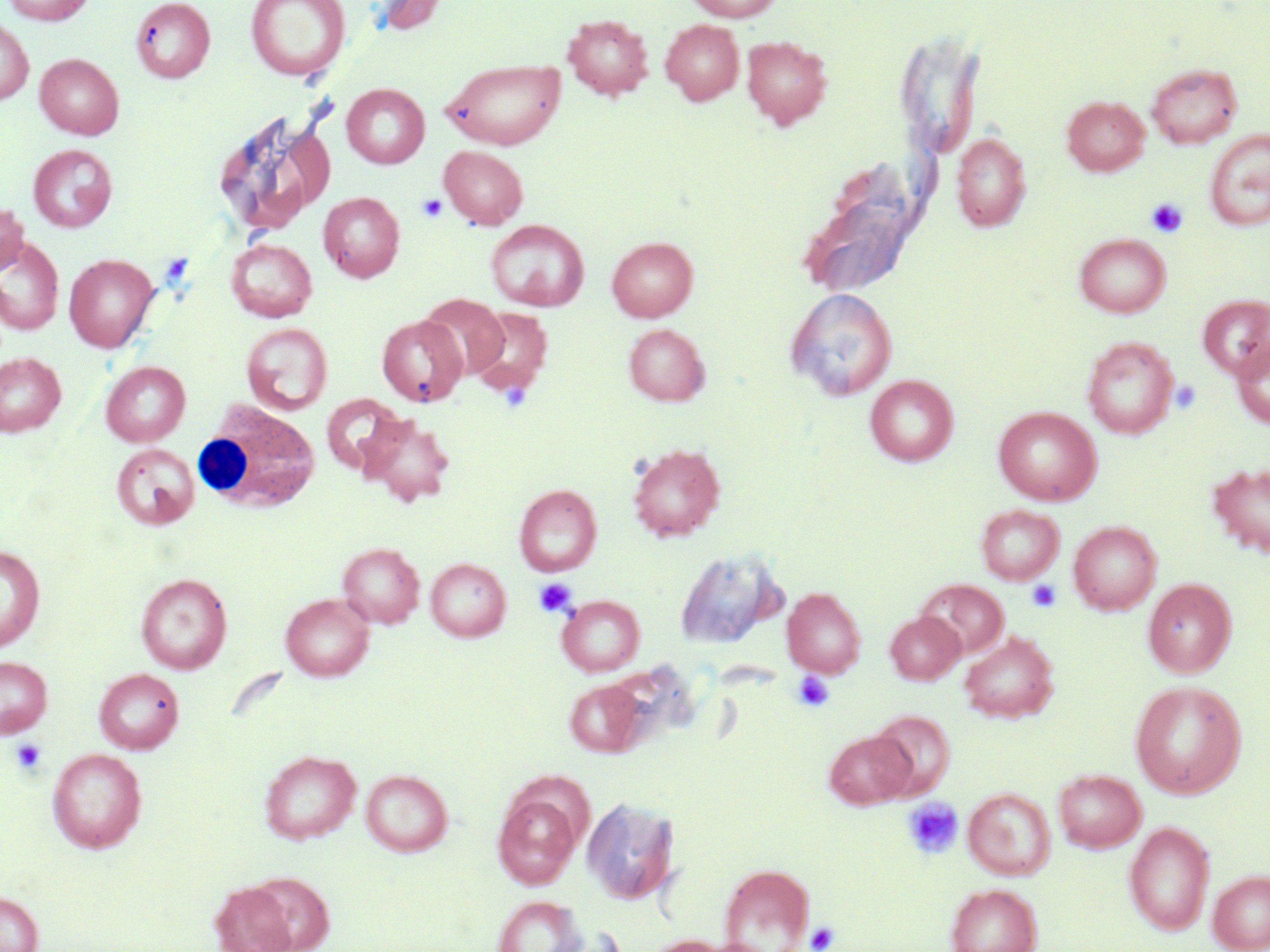
Summary:
  - Coordinate format: approximate bounding boxes as named x1/y1/x2/y2 corners in pixels
  - White blood cell locations: (x1=193, y1=401, x2=321, y2=514)
  - Uninfected red blood cell locations: (x1=2, y1=0, x2=95, y2=25), (x1=130, y1=0, x2=215, y2=82), (x1=245, y1=0, x2=351, y2=82), (x1=367, y1=0, x2=450, y2=36), (x1=684, y1=0, x2=784, y2=22), (x1=562, y1=13, x2=653, y2=99), (x1=0, y1=17, x2=34, y2=105), (x1=661, y1=19, x2=744, y2=105), (x1=741, y1=35, x2=832, y2=129), (x1=35, y1=53, x2=124, y2=139), (x1=441, y1=57, x2=566, y2=149), (x1=1146, y1=63, x2=1243, y2=149), (x1=341, y1=83, x2=430, y2=168), (x1=1062, y1=96, x2=1149, y2=176), (x1=216, y1=111, x2=332, y2=233), (x1=1204, y1=129, x2=1270, y2=231), (x1=951, y1=132, x2=1031, y2=232), (x1=28, y1=144, x2=117, y2=232), (x1=439, y1=145, x2=528, y2=230), (x1=318, y1=192, x2=405, y2=282), (x1=0, y1=203, x2=27, y2=276), (x1=486, y1=220, x2=589, y2=311), (x1=1074, y1=233, x2=1171, y2=318), (x1=0, y1=235, x2=65, y2=336), (x1=607, y1=236, x2=698, y2=321), (x1=227, y1=238, x2=317, y2=321), (x1=65, y1=254, x2=158, y2=352), (x1=786, y1=288, x2=897, y2=401), (x1=420, y1=293, x2=509, y2=379), (x1=1198, y1=294, x2=1270, y2=381), (x1=467, y1=306, x2=554, y2=398), (x1=377, y1=315, x2=467, y2=407), (x1=242, y1=323, x2=332, y2=415), (x1=624, y1=323, x2=709, y2=405), (x1=1082, y1=336, x2=1179, y2=439), (x1=1232, y1=336, x2=1270, y2=430), (x1=0, y1=352, x2=66, y2=436), (x1=101, y1=361, x2=190, y2=446), (x1=865, y1=375, x2=958, y2=466), (x1=320, y1=394, x2=404, y2=475), (x1=993, y1=406, x2=1102, y2=505), (x1=358, y1=414, x2=455, y2=507), (x1=111, y1=443, x2=200, y2=531), (x1=628, y1=443, x2=725, y2=541), (x1=1207, y1=462, x2=1270, y2=560), (x1=514, y1=484, x2=602, y2=576), (x1=976, y1=505, x2=1065, y2=584), (x1=1068, y1=521, x2=1161, y2=615), (x1=337, y1=542, x2=425, y2=628), (x1=0, y1=544, x2=45, y2=652), (x1=675, y1=550, x2=784, y2=650), (x1=425, y1=558, x2=511, y2=642), (x1=136, y1=573, x2=232, y2=673), (x1=1143, y1=578, x2=1236, y2=677), (x1=918, y1=579, x2=1009, y2=659), (x1=782, y1=586, x2=866, y2=677), (x1=281, y1=593, x2=374, y2=681), (x1=557, y1=595, x2=644, y2=675), (x1=885, y1=612, x2=965, y2=684), (x1=959, y1=631, x2=1058, y2=722), (x1=0, y1=656, x2=52, y2=738), (x1=94, y1=667, x2=184, y2=754), (x1=564, y1=679, x2=647, y2=757), (x1=1129, y1=680, x2=1248, y2=799), (x1=869, y1=710, x2=955, y2=799), (x1=823, y1=730, x2=915, y2=809), (x1=47, y1=747, x2=148, y2=853), (x1=260, y1=749, x2=361, y2=844), (x1=361, y1=768, x2=453, y2=856), (x1=1053, y1=769, x2=1147, y2=853), (x1=963, y1=788, x2=1056, y2=880), (x1=494, y1=793, x2=580, y2=889), (x1=582, y1=798, x2=680, y2=904), (x1=1123, y1=821, x2=1215, y2=934), (x1=718, y1=863, x2=814, y2=951), (x1=1208, y1=869, x2=1270, y2=952), (x1=247, y1=871, x2=335, y2=951), (x1=210, y1=882, x2=297, y2=952), (x1=945, y1=883, x2=1042, y2=952), (x1=0, y1=891, x2=43, y2=952), (x1=493, y1=895, x2=585, y2=952), (x1=645, y1=935, x2=730, y2=952)
  - Platelet locations: (x1=416, y1=194, x2=447, y2=222), (x1=1146, y1=198, x2=1188, y2=237), (x1=1170, y1=380, x2=1201, y2=414), (x1=534, y1=577, x2=577, y2=617), (x1=1026, y1=579, x2=1062, y2=613), (x1=793, y1=671, x2=834, y2=711), (x1=10, y1=738, x2=47, y2=775), (x1=901, y1=797, x2=963, y2=859), (x1=805, y1=921, x2=840, y2=951)
  - Slide-level diagnosis: no evidence of blood parasites
  - Stain: May-Grünwald-Giemsa
  - Field of view: single
  - Preparation: thin blood film
  - Image size: 1270×952 pixels
  - Magnification: 1000x
  - Modality: optical microscopy